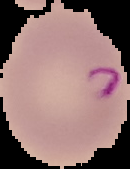
Summary:
  - Image type: cell region segmented out of the field of view; surrounding area masked to black
  - Image size: 130×169 pixels
  - Preparation: thin blood smear
  - Malaria status: parasitized